Locate every Plasmodium parasite.
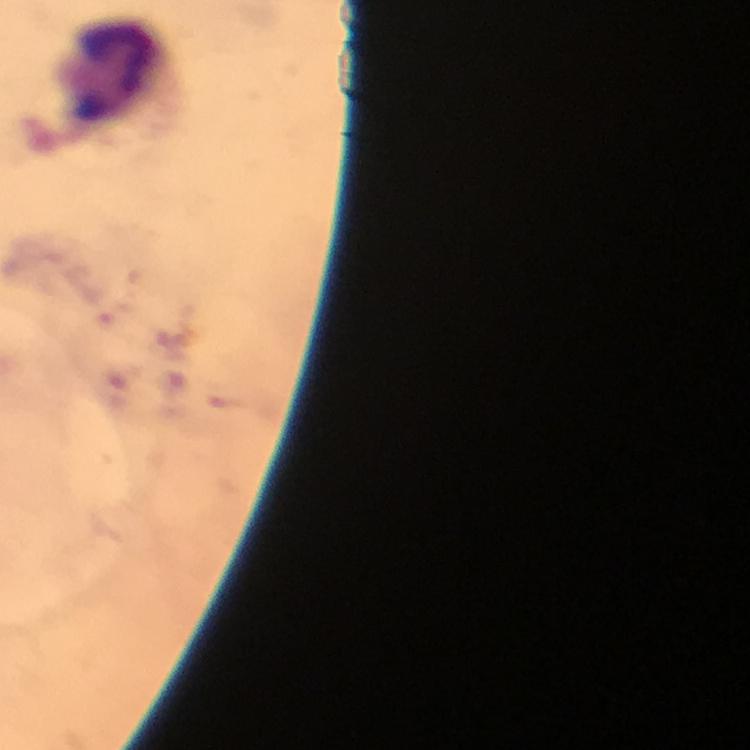

No Plasmodium parasites detected.

context = from a malaria diagnostic workup
stain = Giemsa
capture = smartphone mounted on the microscope
cropped from = one field of view
magnification = 100x
image size = 750×750 pixels
leukocyte locations = approximate centers as [x, y] in pixels: [118, 74]
preparation = thick blood film
immersion oil = applied